Classify this cell by malaria status.
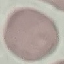
It is uninfected.

Giemsa stain. Cell patch, automatically extracted from a larger field of view and resized to 64 × 64 pixels. Thin smear of blood. Photographed with a smartphone camera at the microscope eyepiece.